Report the malaria status of this cell.
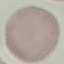

It is uninfected.

Giemsa stain. Acquired by smartphone through the microscope eyepiece. Thin smear of blood. Cell patch, automatically extracted from a larger field of view and resized to 64 × 64 pixels.